Name the cell type shown.
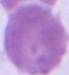
This is an erythrocyte.

modality = photomicrograph
magnification = 1000x